Assess this cell for malaria.
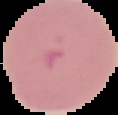
Parasitized.

{
  "image_size": "118×115 pixels",
  "preparation": "thin blood film",
  "image_type": "segmented cell region on a black background"
}